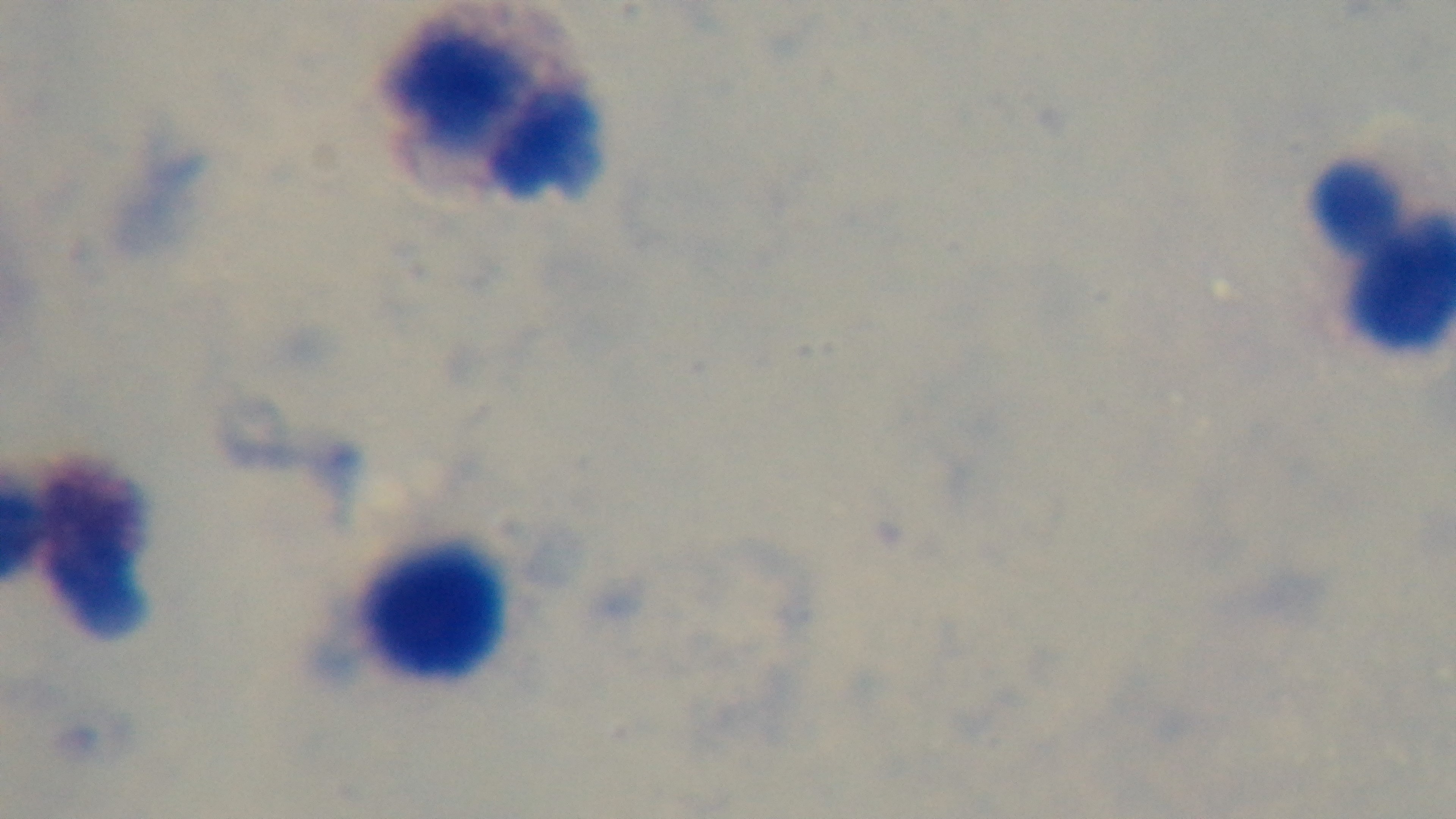
Summary:
  - Objective: 100x oil immersion
  - Preparation: thick blood film
  - Capture: mounted 4K digital camera
  - Modality: light microscopy
  - Stain: Giemsa
  - Malaria status: negative
  - Field of view: one from the slide